Classify this cell by malaria status.
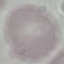

Uninfected.

stain = Giemsa
capture = smartphone through the microscope eyepiece
image type = automatically extracted cell patch, resized to 64 × 64 pixels
preparation = thin blood smear